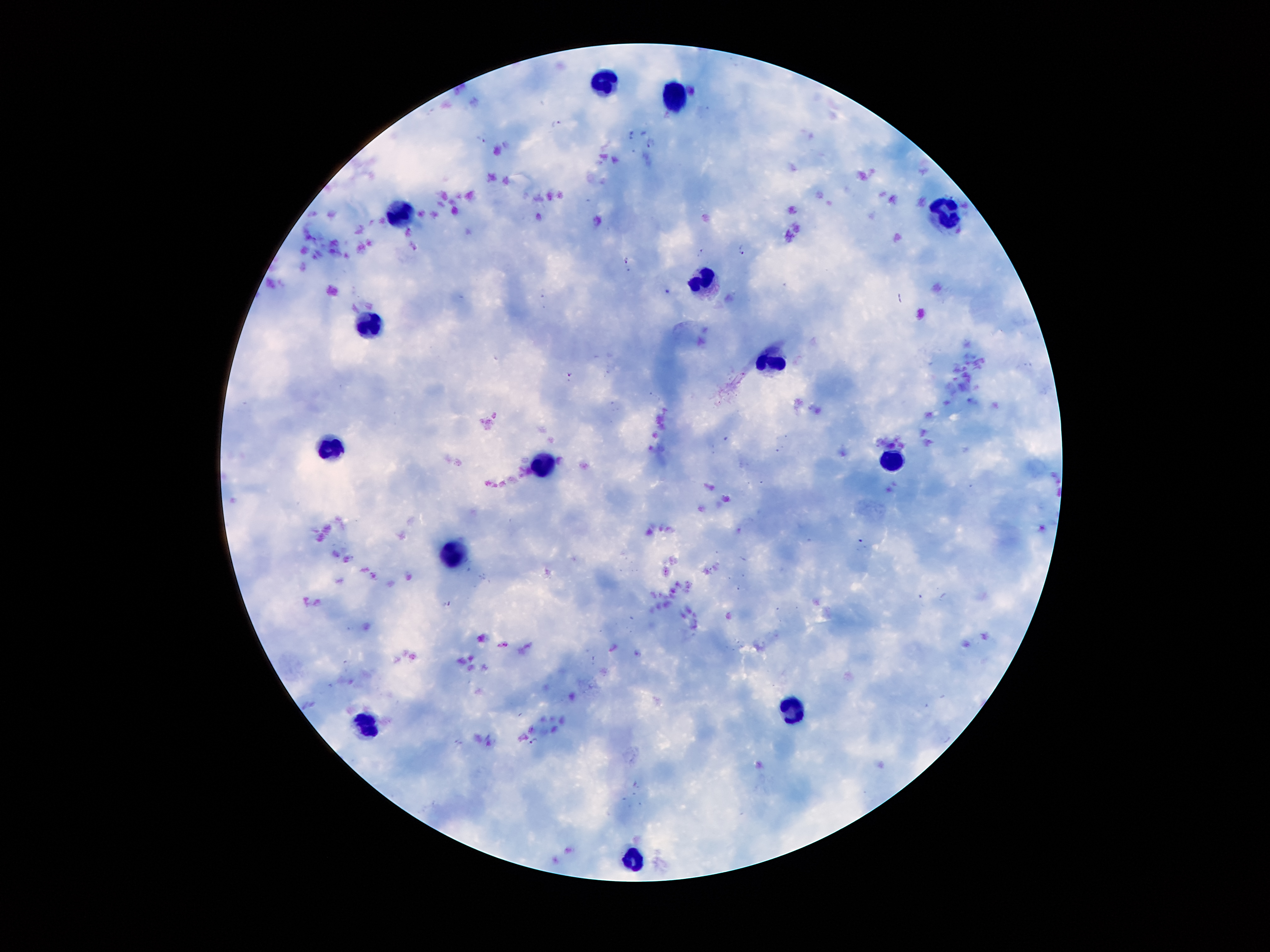

Approximate centers as [x, y] in pixels.
Summary:
  - Leukocyte locations: [599, 85], [672, 100], [942, 213], [393, 216], [704, 278], [369, 328], [764, 362], [325, 451], [890, 465], [539, 466], [452, 557], [793, 708], [369, 730], [630, 858]
  - Plasmodium parasite locations: [556, 123], [631, 133], [481, 139], [650, 144], [743, 251], [701, 252], [626, 261], [667, 293], [570, 375], [860, 544], [446, 607], [534, 740]
  - Patient malaria status: infected with Plasmodium falciparum
  - Stain: Giemsa
  - Image size: 1270×952 pixels
  - Preparation: thick peripheral-blood smear
  - Field of view: single
  - Magnification: 100x
  - Capture: smartphone through the microscope eyepiece